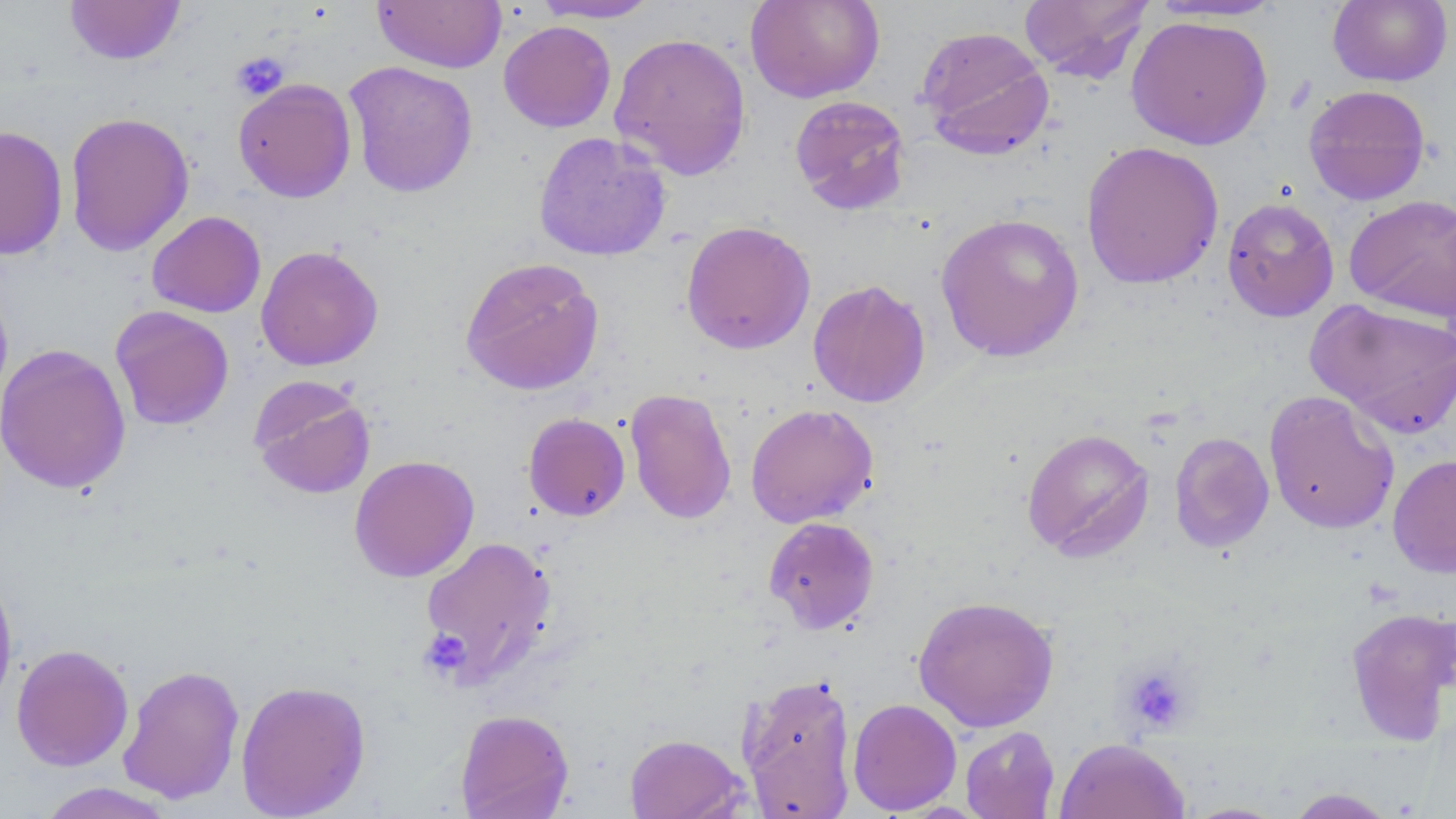
Approximate bounding boxes as [x1, y1, x2, y2] in pixels. Uninfected red blood cell locations: [64, 0, 186, 65], [530, 0, 664, 23], [745, 0, 885, 103], [1018, 0, 1154, 83], [1147, 0, 1285, 23], [1327, 0, 1453, 87], [371, 1, 506, 73], [1125, 15, 1273, 150], [499, 20, 616, 133], [915, 25, 1055, 161], [609, 31, 751, 180], [343, 61, 479, 198], [233, 78, 357, 203], [1303, 84, 1431, 205], [789, 95, 911, 216], [64, 111, 195, 257], [0, 125, 68, 261], [533, 131, 672, 261], [1080, 140, 1224, 289], [1344, 194, 1456, 322], [1222, 196, 1339, 322], [146, 211, 266, 318], [935, 212, 1085, 362], [680, 220, 816, 355], [255, 245, 384, 371], [459, 256, 605, 396], [0, 276, 13, 411], [807, 279, 931, 408], [1306, 298, 1456, 437], [110, 305, 234, 430], [0, 342, 131, 495], [248, 377, 375, 500], [624, 387, 738, 525], [1263, 389, 1400, 535], [745, 403, 879, 528], [523, 412, 630, 521], [1021, 427, 1155, 562], [1169, 432, 1275, 553], [1388, 453, 1456, 579], [349, 454, 480, 582], [763, 516, 880, 634], [419, 535, 558, 688], [0, 566, 18, 717], [913, 594, 1060, 733], [1344, 606, 1456, 745], [11, 643, 134, 771], [117, 664, 245, 805], [737, 672, 858, 817], [235, 679, 371, 818], [847, 697, 962, 815], [455, 708, 574, 819], [960, 726, 1060, 818], [624, 733, 747, 819], [1054, 738, 1191, 819], [34, 782, 179, 819], [1284, 787, 1399, 818], [1179, 801, 1290, 818]. Platelet locations: [232, 52, 289, 101], [419, 629, 471, 679], [1119, 663, 1194, 735]. Slide-level diagnosis: no evidence of blood parasites. One field of a larger specimen. Thin blood smear. May-Grünwald-Giemsa-stained preparation. 1000x magnification. Image is 1456×819 pixels. Light microscopy.